Report the malaria status of this cell.
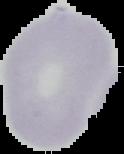

It is uninfected.

Image is 124×154 pixels. From a thin blood smear. The area outside the segmented cell region is set to black.